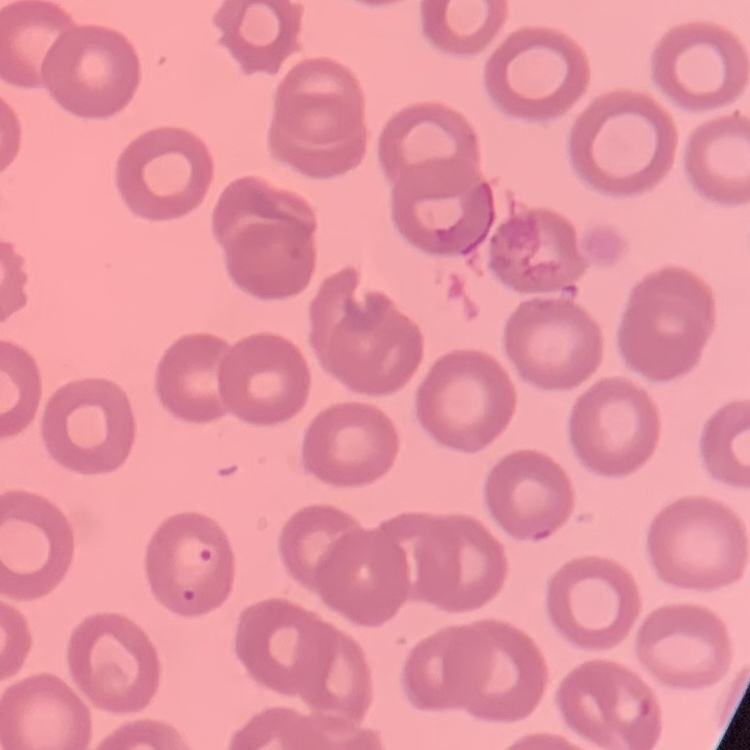

erythrocyte morphology = no rouleaux formation
image type = square crop of a larger photomicrograph
preparation = thin blood film
stain = Field's or Giemsa